Report the malaria status of this cell.
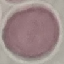
Uninfected.

Acquired by smartphone through the microscope eyepiece. Giemsa-stained preparation. Thin blood smear. Automatically extracted cell patch, resized to 64 × 64 pixels.